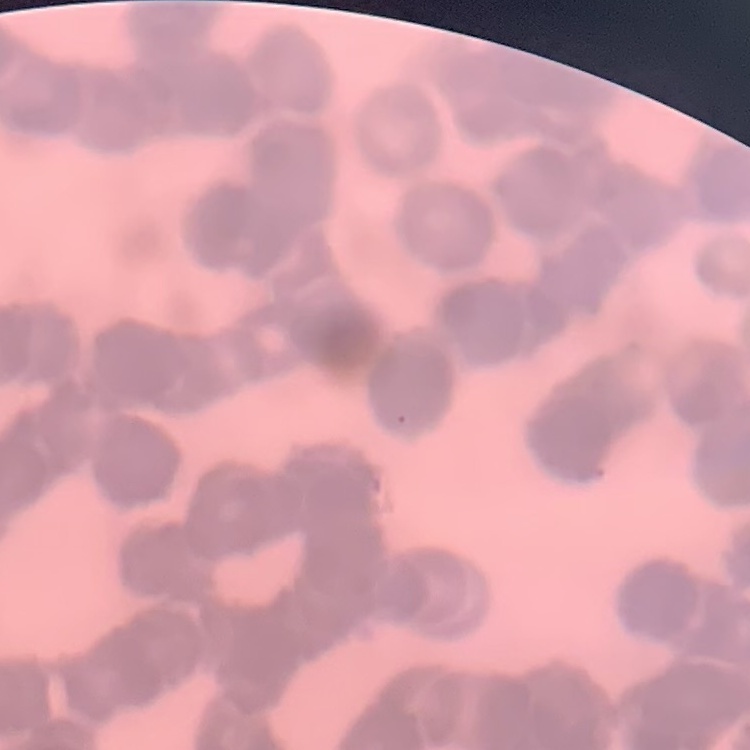
The red blood cells exhibit rouleaux formation. Field's or Giemsa stain. Square crop of a larger photomicrograph. Thin blood smear.